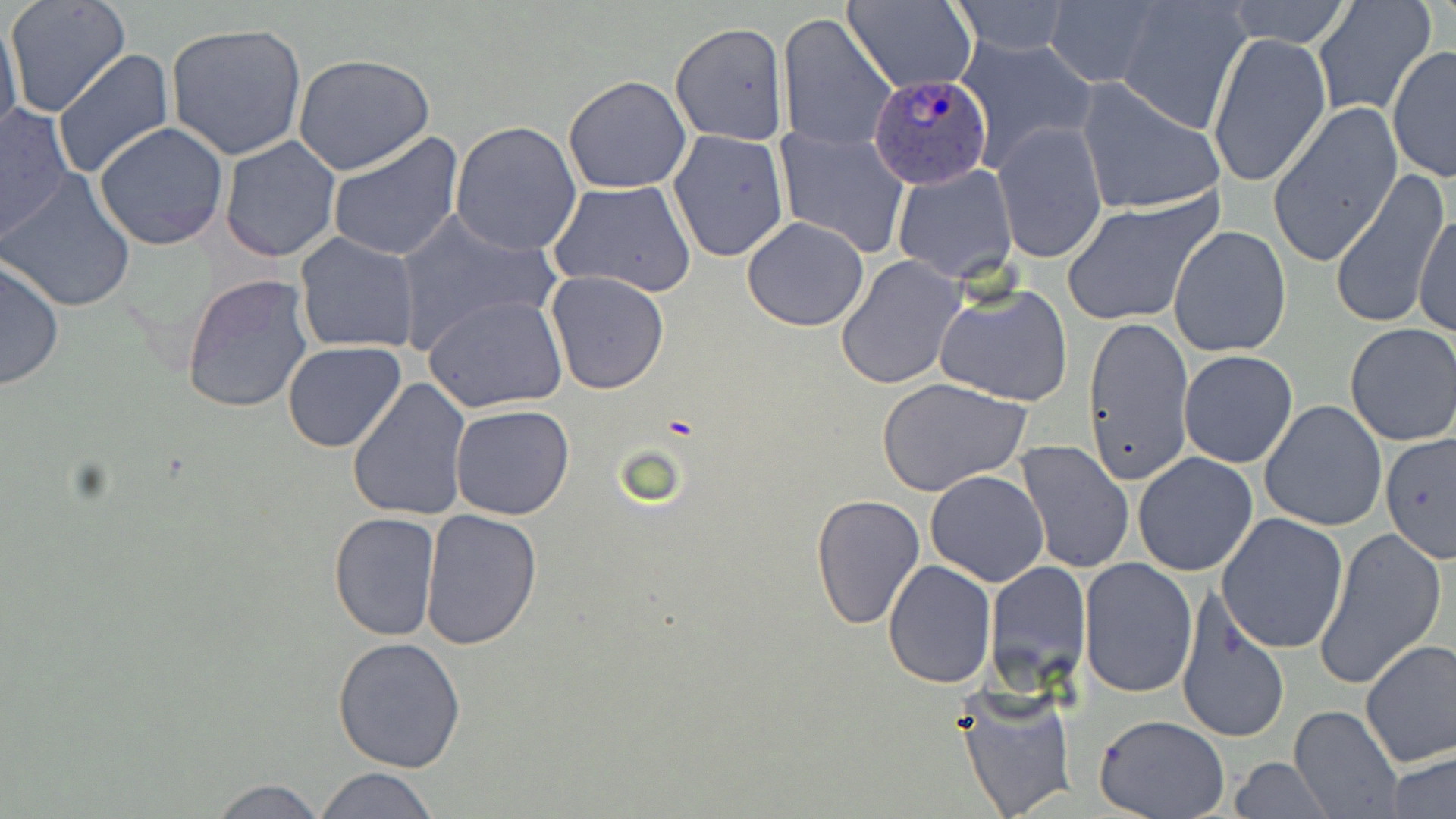

Summary:
  - Coordinate format: approximate bounding boxes as [x1, y1, x2, y2] in pixels
  - Uninfected red blood cell locations: [6, 0, 132, 119], [1313, 0, 1437, 117], [841, 1, 976, 95], [947, 1, 1074, 54], [1043, 1, 1162, 88], [1120, 1, 1249, 131], [1222, 1, 1354, 48], [777, 12, 893, 152], [0, 18, 22, 136], [670, 23, 787, 145], [165, 24, 306, 160], [1208, 31, 1329, 190], [954, 32, 1098, 173], [1387, 46, 1456, 181], [53, 49, 174, 179], [293, 54, 437, 176], [563, 76, 692, 192], [1073, 80, 1226, 215], [1269, 101, 1403, 267], [0, 104, 74, 242], [450, 120, 583, 254], [994, 120, 1108, 265], [92, 121, 230, 250], [773, 127, 910, 257], [667, 129, 789, 263], [325, 131, 464, 263], [220, 136, 341, 262], [892, 165, 1017, 283], [1329, 170, 1450, 331], [2, 171, 138, 314], [549, 179, 698, 297], [1059, 193, 1222, 328], [1415, 210, 1454, 339], [394, 213, 560, 351], [740, 216, 871, 331], [1168, 225, 1292, 357], [293, 233, 419, 354], [0, 255, 67, 394], [838, 257, 966, 390], [546, 271, 669, 394], [180, 275, 313, 415], [933, 283, 1075, 407], [425, 294, 568, 415], [1082, 315, 1194, 487], [1343, 323, 1456, 447], [282, 341, 407, 453], [1177, 347, 1300, 469], [347, 376, 472, 524], [879, 379, 1031, 497], [1258, 399, 1387, 532], [450, 404, 575, 520], [1379, 432, 1456, 563], [1015, 439, 1134, 575], [1132, 451, 1259, 577], [924, 470, 1050, 587], [810, 493, 926, 629], [419, 508, 542, 649], [327, 511, 441, 641], [1215, 513, 1349, 654], [1313, 524, 1449, 690], [883, 558, 996, 687], [1078, 558, 1198, 699], [986, 559, 1090, 686], [1173, 592, 1290, 746], [332, 635, 467, 775], [1359, 638, 1456, 768], [956, 686, 1079, 819], [1289, 704, 1403, 819], [1093, 714, 1230, 819], [1384, 750, 1455, 819], [1227, 758, 1336, 817], [309, 766, 440, 819], [202, 777, 334, 818]
  - Plasmodium ovale-infected red blood cell locations: [869, 71, 994, 197]
  - Slide-level diagnosis: Plasmodium ovale
  - Magnification: 1000x
  - Field of view: single
  - Preparation: thin blood film
  - Modality: light microscopy
  - Image size: 1456×819 pixels
  - Stain: May-Grünwald-Giemsa